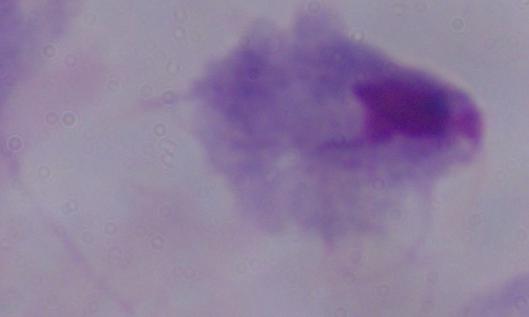 A trichomonad is shown. Captured at 1000x magnification. Micrograph.